Evaluate for Plasmodium parasites.
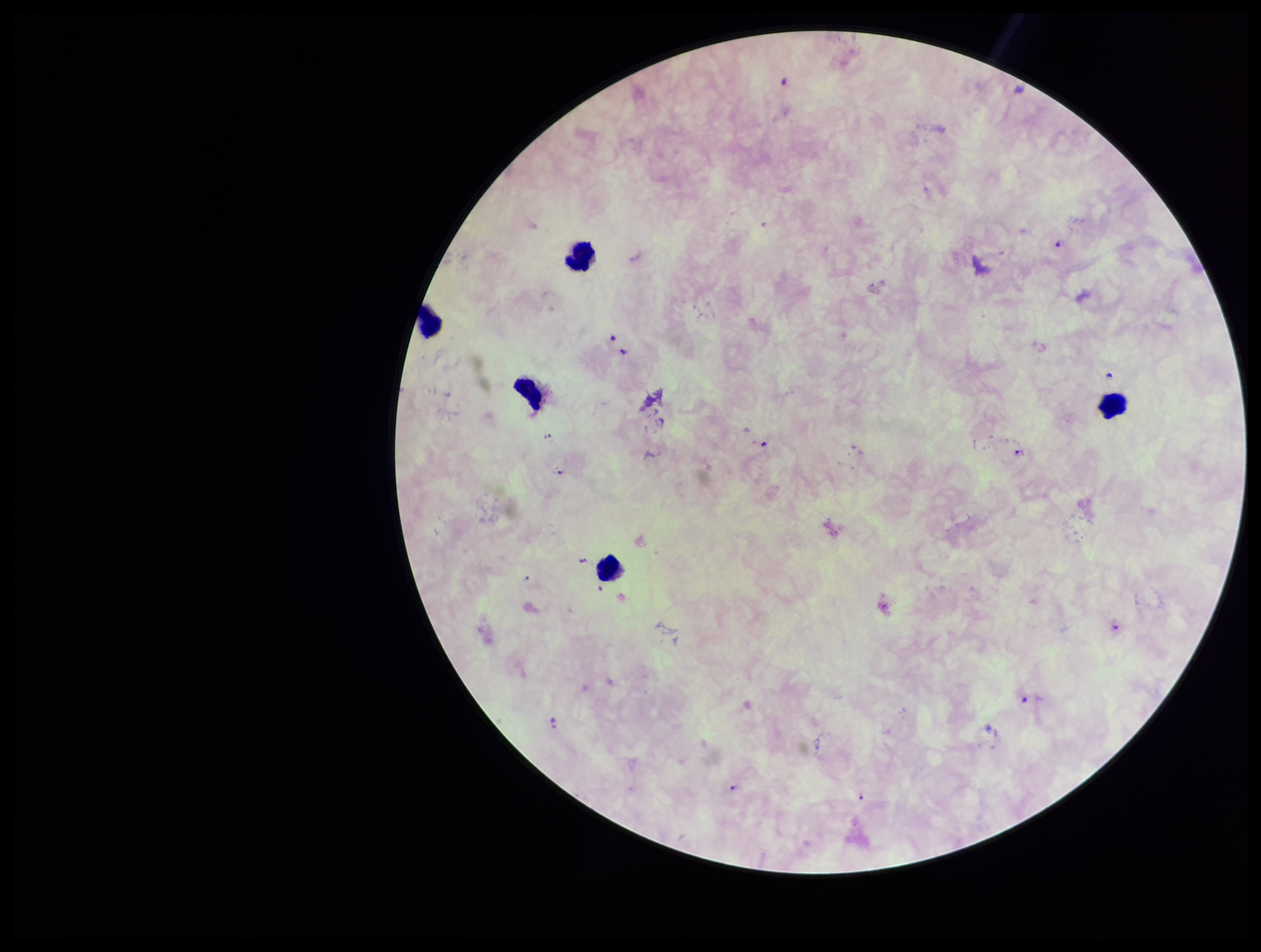

Seen.

Parasite count: 11. Species reported for this patient: Plasmodium falciparum. Preparation: thick. Leukocyte count: 5. Single field of view. Stained with Giemsa. Image is 1261×952 pixels. Patient malaria status: infected. Smartphone photograph taken through the eyepiece of a microscope.